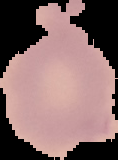

preparation: thin blood film
image_type: cell region segmented out of the field of view; surrounding area masked to black
image_size: 118×160 pixels
malaria_status: uninfected